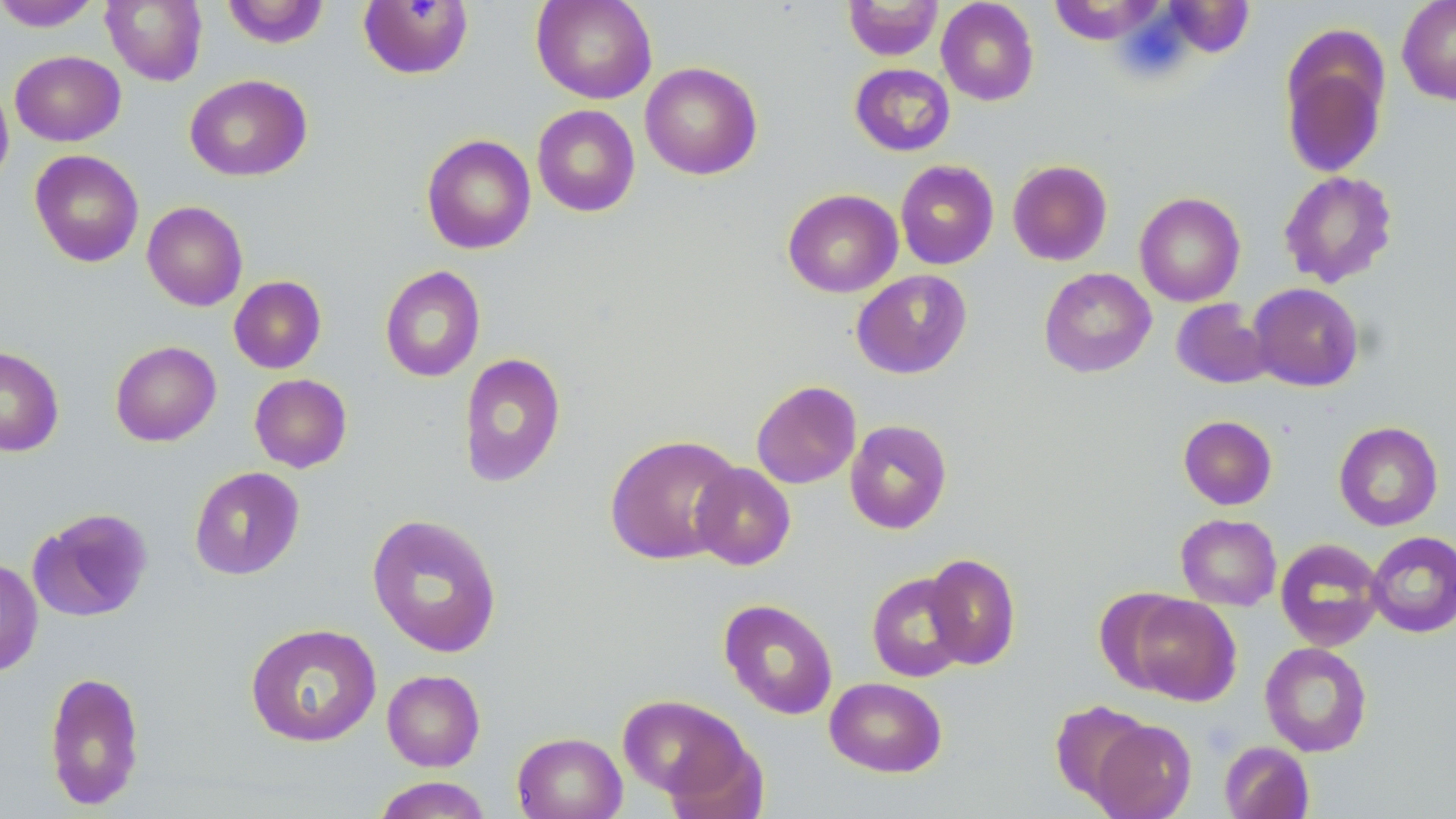
Summary:
  - Coordinate format: approximate bounding boxes as named x1/y1/x2/y2 corners in pixels
  - Uninfected red blood cell locations: (x1=101, y1=0, x2=208, y2=86), (x1=221, y1=0, x2=330, y2=48), (x1=531, y1=0, x2=657, y2=104), (x1=843, y1=0, x2=943, y2=60), (x1=936, y1=0, x2=1039, y2=106), (x1=1397, y1=0, x2=1456, y2=105), (x1=0, y1=1, x2=104, y2=31), (x1=357, y1=1, x2=475, y2=80), (x1=1280, y1=40, x2=1390, y2=179), (x1=10, y1=50, x2=126, y2=146), (x1=640, y1=62, x2=763, y2=180), (x1=849, y1=63, x2=956, y2=156), (x1=185, y1=74, x2=312, y2=181), (x1=0, y1=78, x2=13, y2=190), (x1=532, y1=104, x2=640, y2=217), (x1=421, y1=134, x2=536, y2=254), (x1=29, y1=149, x2=144, y2=267), (x1=1007, y1=159, x2=1112, y2=266), (x1=895, y1=160, x2=998, y2=269), (x1=1279, y1=171, x2=1398, y2=288), (x1=782, y1=189, x2=903, y2=297), (x1=1135, y1=192, x2=1245, y2=306), (x1=142, y1=201, x2=248, y2=311), (x1=379, y1=265, x2=485, y2=382), (x1=1039, y1=267, x2=1156, y2=378), (x1=851, y1=269, x2=973, y2=379), (x1=228, y1=275, x2=327, y2=374), (x1=1248, y1=283, x2=1364, y2=391), (x1=1171, y1=299, x2=1273, y2=390), (x1=110, y1=340, x2=221, y2=447), (x1=0, y1=346, x2=64, y2=456), (x1=458, y1=352, x2=566, y2=487), (x1=249, y1=373, x2=352, y2=473), (x1=751, y1=380, x2=861, y2=489), (x1=1178, y1=415, x2=1277, y2=510), (x1=845, y1=419, x2=952, y2=534), (x1=1334, y1=421, x2=1443, y2=531), (x1=605, y1=434, x2=743, y2=565), (x1=691, y1=462, x2=796, y2=570), (x1=189, y1=466, x2=305, y2=580), (x1=26, y1=507, x2=153, y2=622), (x1=366, y1=513, x2=503, y2=658), (x1=1176, y1=514, x2=1282, y2=610), (x1=1366, y1=531, x2=1456, y2=637), (x1=1275, y1=538, x2=1385, y2=651), (x1=923, y1=553, x2=1021, y2=670), (x1=0, y1=557, x2=43, y2=676), (x1=866, y1=572, x2=971, y2=682), (x1=1124, y1=592, x2=1242, y2=706), (x1=719, y1=598, x2=838, y2=720), (x1=245, y1=623, x2=382, y2=748), (x1=1260, y1=642, x2=1372, y2=757), (x1=382, y1=669, x2=485, y2=772), (x1=43, y1=671, x2=146, y2=810), (x1=824, y1=676, x2=947, y2=777), (x1=617, y1=694, x2=751, y2=801), (x1=1049, y1=700, x2=1153, y2=805), (x1=1088, y1=719, x2=1197, y2=819), (x1=513, y1=731, x2=627, y2=819), (x1=662, y1=731, x2=768, y2=819), (x1=1219, y1=741, x2=1314, y2=819), (x1=372, y1=776, x2=494, y2=818)
  - Slide-level diagnosis: negative for blood parasites
  - Field of view: single
  - Stain: May-Grünwald-Giemsa
  - Preparation: thin blood film
  - Image size: 1456×819 pixels
  - Modality: light microscopy
  - Magnification: 1000x